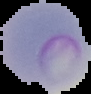
The area outside the segmented cell region is set to black. Image is 91×94 pixels. From a thin blood smear. Result: malaria parasites identified.